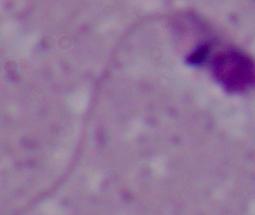 A Leishmania parasite is shown. Micrograph. 1000x magnification.